Assess the morphology of the erythrocytes.
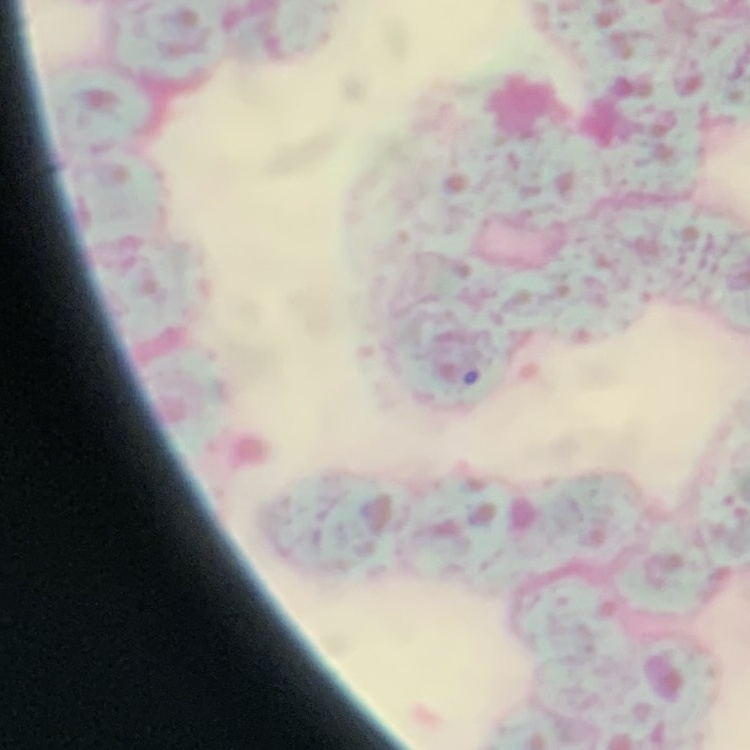

They show rouleaux formation.

image_type: one tile cut from a larger photomicrograph
stain: Field's or Giemsa
preparation: thin blood smear